Identify the parasite.
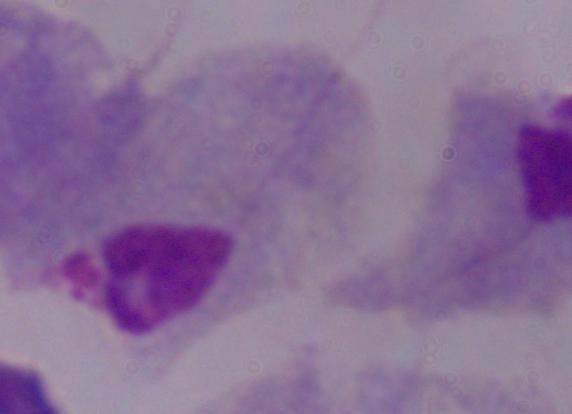

This is a trichomonad.

Micrograph. 1000x magnification.